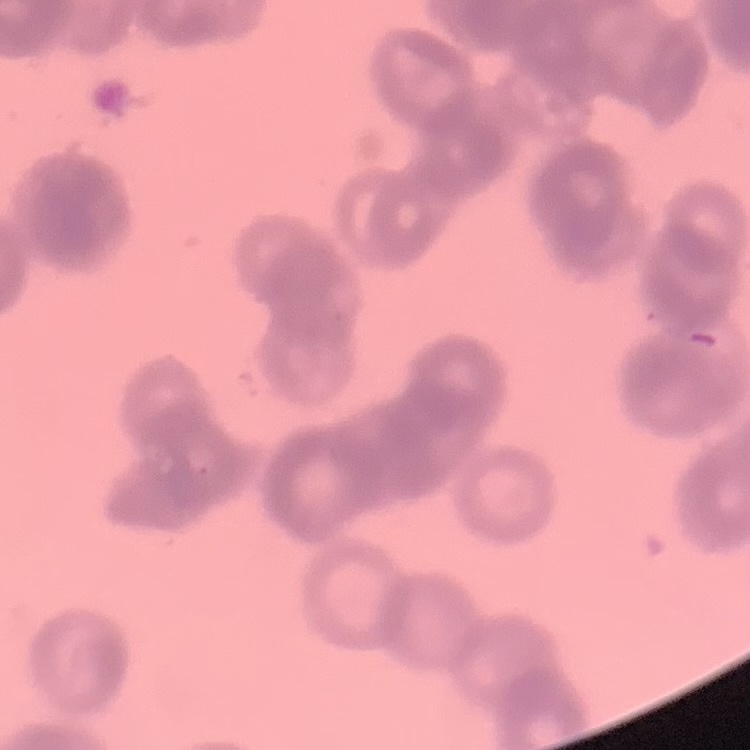

Summary:
  - Red blood cell morphology: rouleaux formation
  - Stain: Field's or Giemsa
  - Image type: square crop of a larger photomicrograph
  - Preparation: thin blood smear